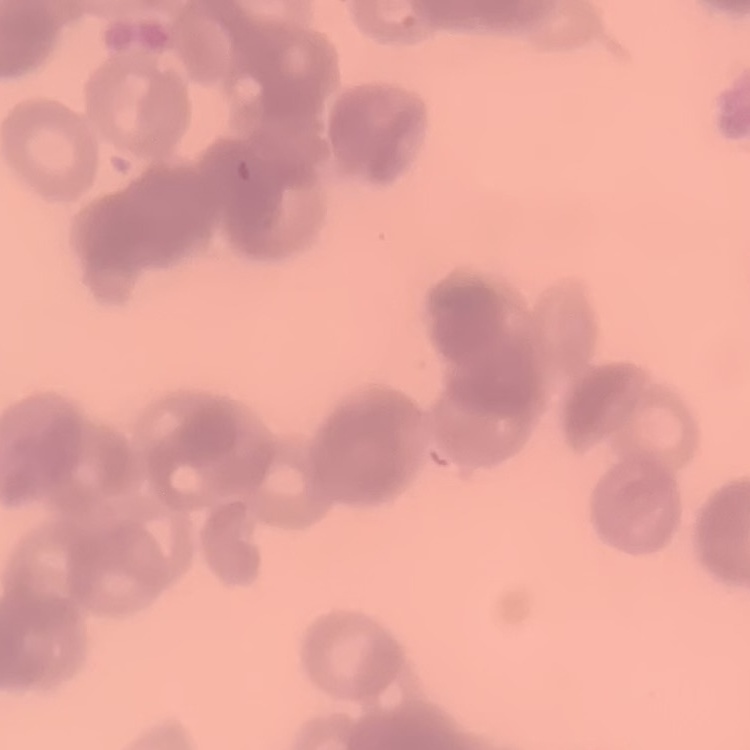
The red blood cells show rouleaux formation. Stained with either Field's or Giemsa. Thin blood film. One tile cut from a larger photomicrograph.